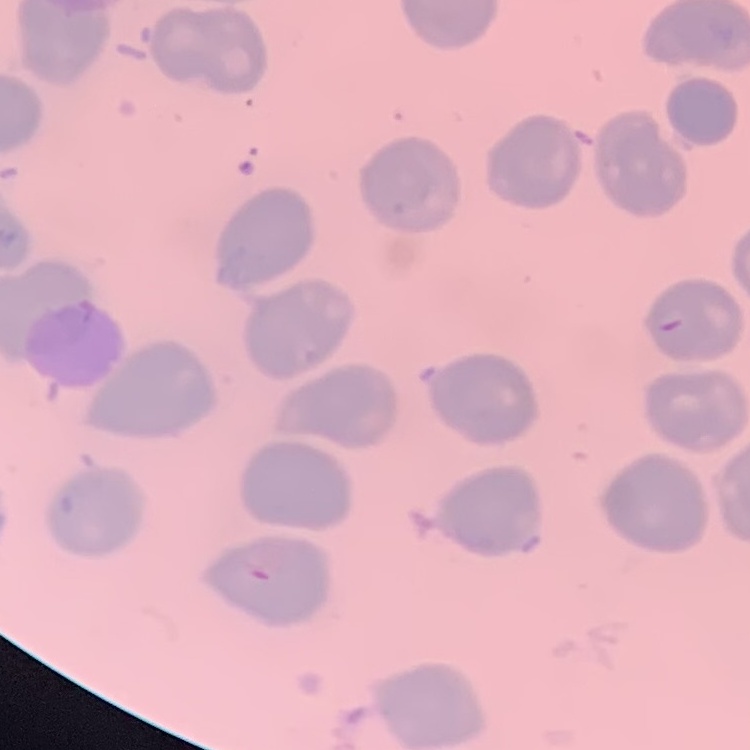

red blood cell morphology = no rouleaux formation
stain = Field's or Giemsa
image type = one tile cut from a larger photomicrograph
preparation = thin peripheral smear